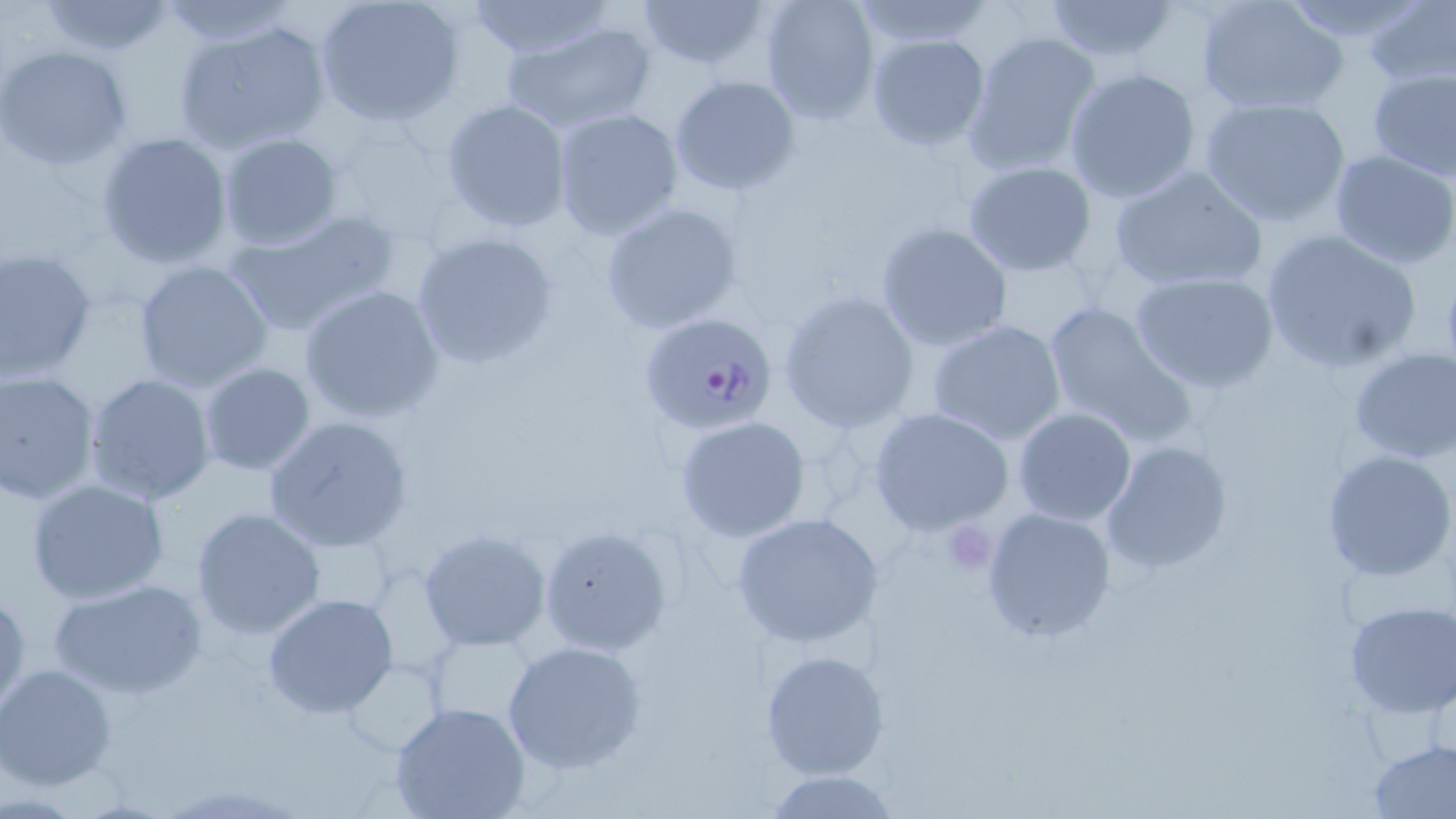

Approximate bounding boxes as named x1/y1/x2/y2 corners in pixels. Uninfected red blood cell locations: (x1=156, y1=0, x2=298, y2=45), (x1=313, y1=0, x2=461, y2=128), (x1=464, y1=0, x2=615, y2=59), (x1=637, y1=0, x2=772, y2=75), (x1=758, y1=0, x2=880, y2=125), (x1=1040, y1=0, x2=1184, y2=66), (x1=1196, y1=0, x2=1348, y2=116), (x1=1276, y1=0, x2=1434, y2=47), (x1=33, y1=1, x2=180, y2=55), (x1=847, y1=1, x2=995, y2=51), (x1=1362, y1=2, x2=1456, y2=87), (x1=171, y1=17, x2=335, y2=156), (x1=500, y1=19, x2=656, y2=132), (x1=961, y1=30, x2=1103, y2=177), (x1=866, y1=34, x2=992, y2=152), (x1=0, y1=46, x2=133, y2=169), (x1=1366, y1=67, x2=1456, y2=180), (x1=1062, y1=68, x2=1204, y2=203), (x1=668, y1=74, x2=803, y2=195), (x1=1199, y1=94, x2=1351, y2=227), (x1=441, y1=99, x2=571, y2=232), (x1=550, y1=107, x2=685, y2=240), (x1=331, y1=125, x2=452, y2=234), (x1=96, y1=130, x2=235, y2=271), (x1=217, y1=132, x2=345, y2=251), (x1=1328, y1=150, x2=1456, y2=272), (x1=961, y1=162, x2=1098, y2=278), (x1=1106, y1=162, x2=1269, y2=293), (x1=599, y1=199, x2=745, y2=334), (x1=223, y1=208, x2=403, y2=338), (x1=875, y1=221, x2=1014, y2=353), (x1=1258, y1=227, x2=1426, y2=375), (x1=409, y1=231, x2=559, y2=371), (x1=0, y1=246, x2=98, y2=381), (x1=132, y1=260, x2=276, y2=391), (x1=1128, y1=269, x2=1280, y2=394), (x1=299, y1=284, x2=445, y2=423), (x1=779, y1=290, x2=920, y2=433), (x1=1041, y1=300, x2=1197, y2=448), (x1=926, y1=318, x2=1068, y2=446), (x1=1348, y1=347, x2=1456, y2=464), (x1=196, y1=362, x2=318, y2=477), (x1=1, y1=369, x2=102, y2=506), (x1=83, y1=372, x2=218, y2=506), (x1=1012, y1=407, x2=1137, y2=526), (x1=868, y1=408, x2=1017, y2=538), (x1=262, y1=415, x2=415, y2=554), (x1=673, y1=415, x2=813, y2=541), (x1=1101, y1=441, x2=1234, y2=575), (x1=1321, y1=450, x2=1454, y2=582), (x1=24, y1=478, x2=170, y2=605), (x1=189, y1=506, x2=327, y2=640), (x1=980, y1=508, x2=1117, y2=645), (x1=732, y1=512, x2=885, y2=651), (x1=538, y1=525, x2=673, y2=657), (x1=417, y1=528, x2=551, y2=652), (x1=46, y1=577, x2=210, y2=700), (x1=0, y1=588, x2=30, y2=716), (x1=262, y1=594, x2=401, y2=721), (x1=1342, y1=600, x2=1456, y2=717), (x1=425, y1=632, x2=540, y2=734), (x1=500, y1=639, x2=647, y2=775), (x1=759, y1=647, x2=888, y2=782), (x1=0, y1=664, x2=119, y2=790), (x1=388, y1=702, x2=533, y2=819), (x1=1367, y1=738, x2=1456, y2=817), (x1=765, y1=769, x2=900, y2=818). Platelet locations: (x1=941, y1=519, x2=998, y2=577). Plasmodium falciparum-infected red blood cell locations: (x1=638, y1=309, x2=779, y2=436). Slide-level diagnosis: Plasmodium falciparum. Image is 1456×819 pixels. Optical microscopy. Captured at 1000x magnification. One field of a larger specimen. Thin blood smear. May-Grünwald-Giemsa-stained preparation.